Describe the morphology of the erythrocytes.
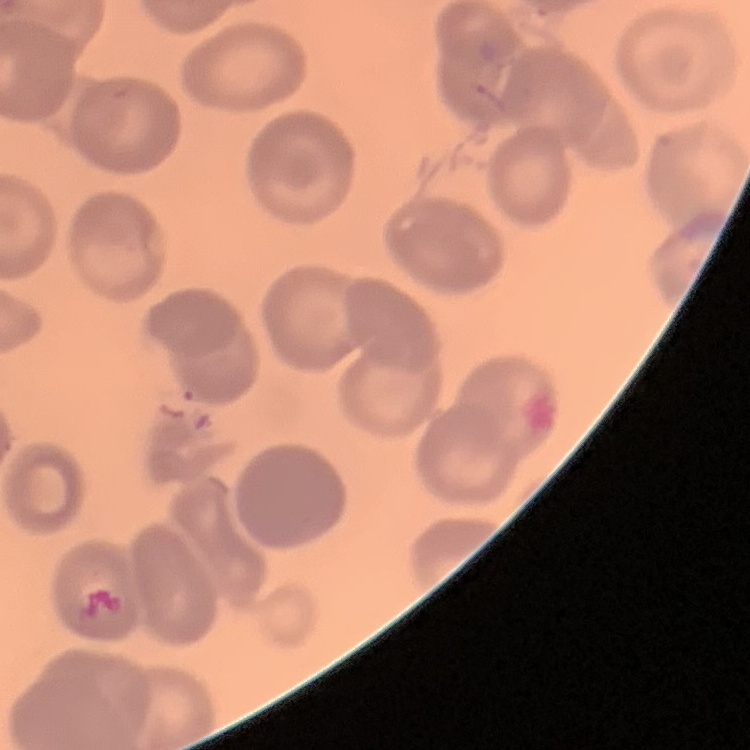

No rouleaux formation.

{
  "preparation": "thin blood smear",
  "stain": "Field's or Giemsa",
  "image_type": "one tile cut from a larger photomicrograph"
}